Locate every malaria parasite.
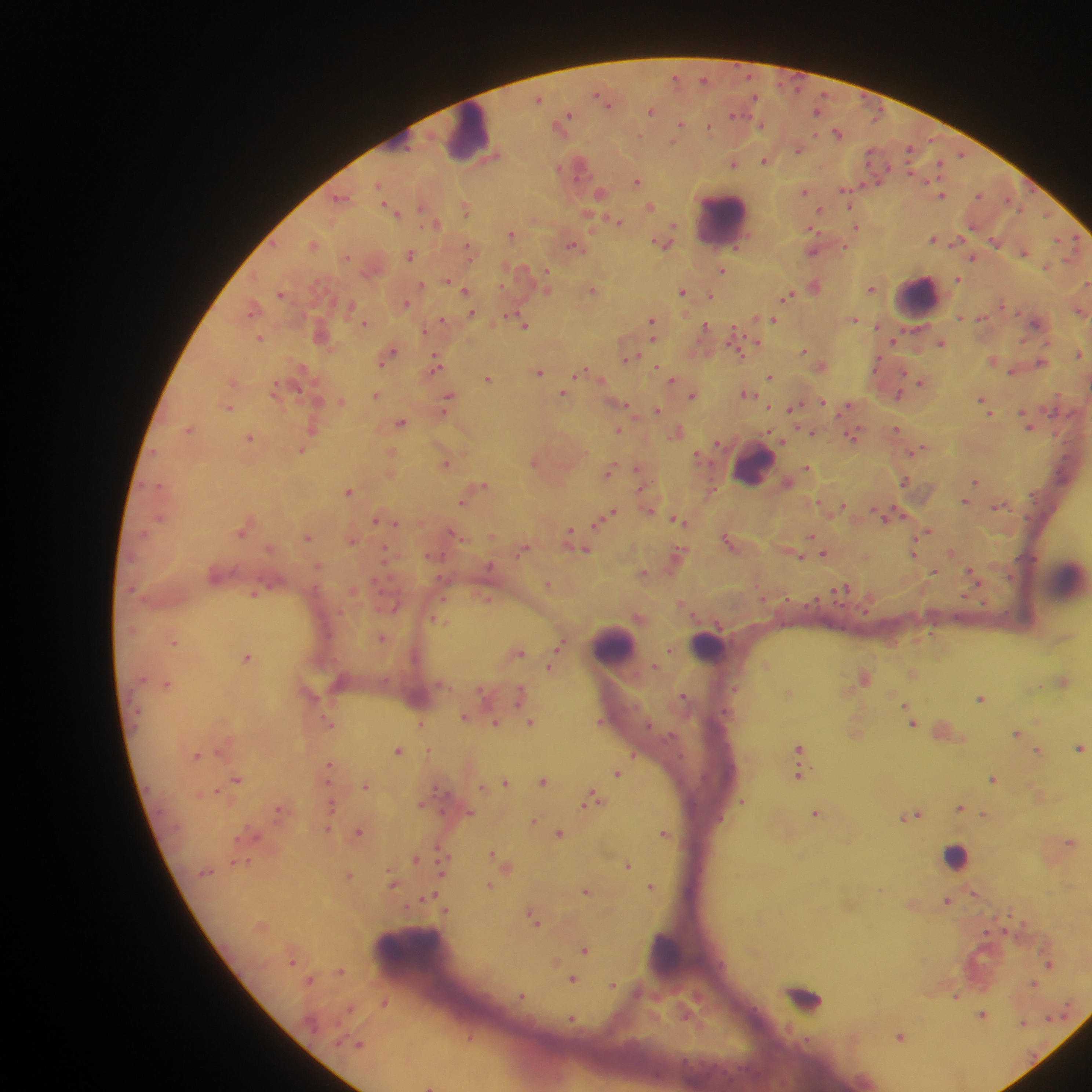

Approximate centers as x y in pixels.
Malaria parasites: 675 77; 704 79; 598 94; 755 97; 539 99; 605 101; 651 111; 817 111; 734 115; 569 116; 565 121; 760 124; 681 125; 709 127; 838 133; 798 150; 910 150; 962 154; 764 161; 734 163; 939 163; 559 168; 637 182; 379 184; 844 188; 805 191; 600 193; 942 195; 978 195; 340 198; 422 206; 650 207; 466 208; 849 208; 820 210; 394 212; 1046 215; 618 221; 437 223; 674 226; 856 227; 813 230; 512 234; 933 239; 958 241; 995 242; 662 243; 313 245; 573 246; 736 247; 469 248; 813 251; 1024 252; 410 256; 347 257; 973 257; 722 271; 546 272; 958 279; 448 280; 1087 283; 422 284; 815 286; 871 289; 466 290; 593 290; 682 291; 281 294; 711 295; 787 295; 406 304; 253 308; 471 313; 960 317; 853 319; 443 320; 774 320; 652 321; 365 323; 1035 324; 525 326; 653 328; 705 328; 877 328; 733 332; 260 338; 653 338; 894 341; 941 342; 757 343; 737 348; 804 350; 1079 353; 741 354; 389 355; 627 358; 992 359; 877 361; 435 362; 1041 362; 658 367; 1012 371; 539 372; 582 373; 770 376; 489 379; 672 379; 920 382; 275 391; 564 393; 746 393; 376 395; 692 395; 899 395; 449 397; 341 401; 983 401; 824 402; 626 405; 847 406; 229 408; 445 408; 793 408; 657 410; 988 410; 1025 414; 401 423; 1029 426; 313 428; 189 429; 896 429; 619 430; 677 432; 812 432; 853 435; 251 438; 782 440; 717 443; 918 450; 301 451; 391 453; 446 464; 807 467; 637 469; 609 471; 905 481; 976 482; 484 484; 348 491; 965 501; 462 502; 819 503; 843 506; 999 506; 649 510; 898 511; 613 513; 882 515; 604 516; 160 517; 678 519; 375 520; 599 521; 396 523; 929 530; 241 531; 569 532; 455 534; 492 535; 811 536; 307 537; 726 538; 352 541; 523 550; 679 550; 585 551; 386 552; 914 552; 825 553; 801 557; 490 566; 643 572; 934 572; 972 573; 548 584; 843 589; 253 594; 965 596; 786 598; 486 600; 984 602; 395 608; 866 612; 382 637; 174 642; 561 645; 669 650; 519 652; 247 657; 766 664; 655 665; 550 667; 1064 680; 167 684; 483 692; 519 695; 683 695; 981 698; 905 705; 464 716; 496 722; 531 722; 600 722; 330 724; 421 724; 912 724; 1017 732; 798 747; 1080 747; 398 750; 1038 751; 197 755; 633 756; 328 766; 618 774; 799 775; 238 779; 993 780; 543 781; 506 782; 366 786; 216 791; 592 799; 742 802; 332 806; 960 808; 278 810; 470 812; 816 813; 917 815; 983 815; 532 822; 328 828; 359 832; 663 833; 559 834; 1071 842; 493 854; 416 859; 246 862; 628 865; 443 872; 348 875; 392 884; 490 885; 651 886; 586 890; 974 893; 429 897; 947 901; 534 920; 585 949; 1050 965; 341 972; 573 980; 1034 984; 613 986; 521 996; 956 996; 384 1003; 349 1009; 982 1015; 1050 1018; 573 1020; 1023 1023; 900 1036; 360 1045; 430 1086.

Summary:
  - Leukocyte locations: 469 135; 722 220; 918 298; 753 466; 1067 577; 614 645; 709 646; 958 856; 668 950; 409 962
  - Image size: 1092×1092 pixels
  - Preparation: thick blood film
  - Capture: mobile-phone photograph through a microscope
  - Field of view: single
  - Country: Ghana